Outline each Plasmodium malariae-infected red blood cell.
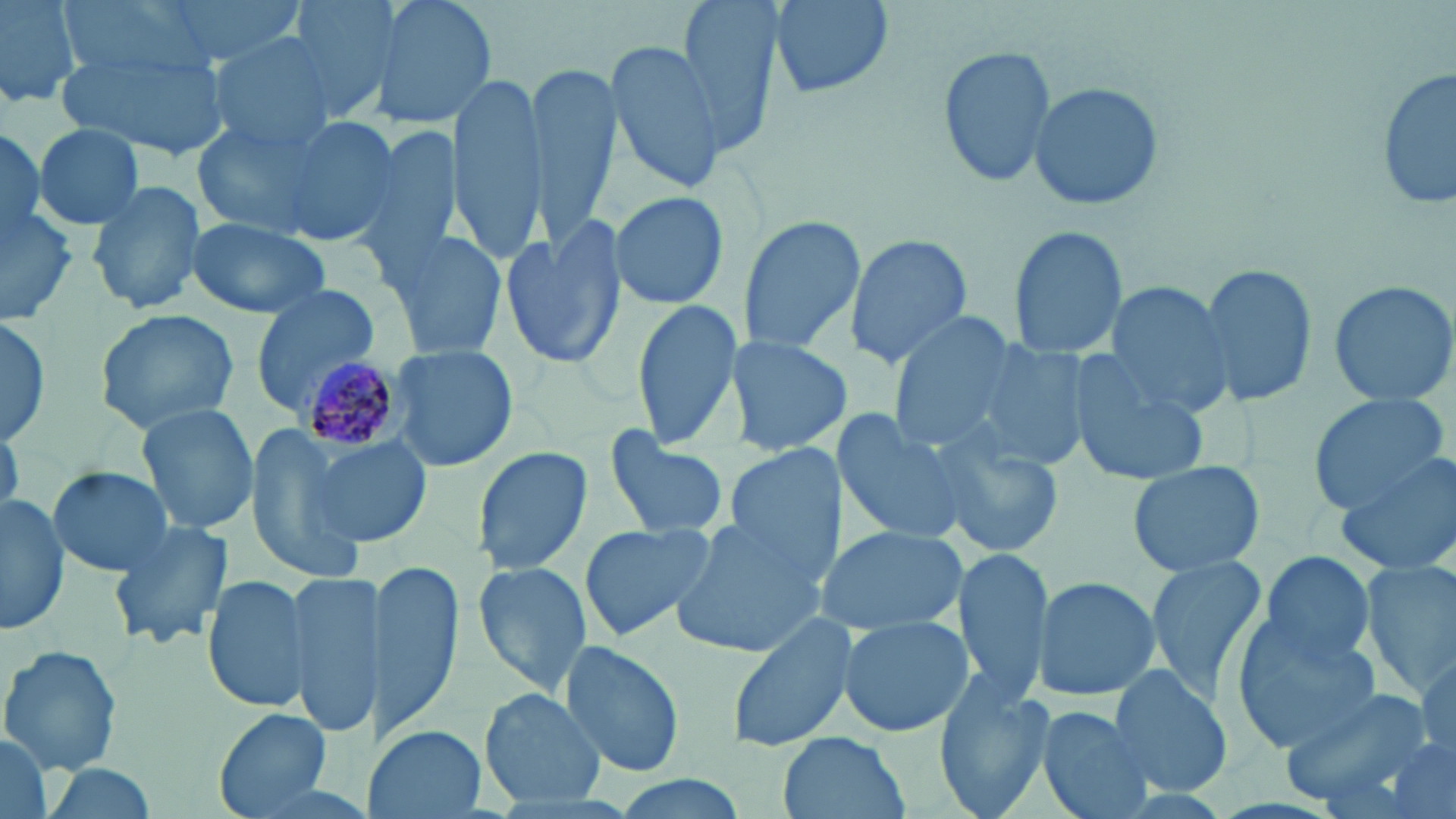

Approximate bounding boxes as named x1/y1/x2/y2 corners in pixels.
Plasmodium malariae-infected red blood cells: (x1=296, y1=355, x2=409, y2=459).

Summary:
  - Uninfected red blood cell locations: (x1=0, y1=0, x2=82, y2=109), (x1=150, y1=0, x2=309, y2=65), (x1=281, y1=0, x2=406, y2=122), (x1=365, y1=0, x2=497, y2=133), (x1=676, y1=0, x2=787, y2=154), (x1=766, y1=0, x2=897, y2=100), (x1=57, y1=35, x2=230, y2=164), (x1=207, y1=35, x2=339, y2=152), (x1=603, y1=36, x2=731, y2=193), (x1=937, y1=45, x2=1058, y2=186), (x1=525, y1=64, x2=618, y2=244), (x1=1377, y1=67, x2=1456, y2=215), (x1=447, y1=71, x2=547, y2=258), (x1=1027, y1=82, x2=1166, y2=212), (x1=192, y1=117, x2=333, y2=240), (x1=269, y1=117, x2=404, y2=249), (x1=353, y1=121, x2=463, y2=276), (x1=0, y1=123, x2=47, y2=243), (x1=32, y1=123, x2=146, y2=230), (x1=87, y1=178, x2=208, y2=317), (x1=609, y1=189, x2=730, y2=312), (x1=0, y1=203, x2=79, y2=322), (x1=735, y1=212, x2=867, y2=357), (x1=499, y1=216, x2=628, y2=372), (x1=185, y1=219, x2=332, y2=319), (x1=1007, y1=225, x2=1129, y2=359), (x1=381, y1=228, x2=509, y2=360), (x1=843, y1=233, x2=972, y2=369), (x1=1199, y1=263, x2=1317, y2=407), (x1=1326, y1=278, x2=1456, y2=405), (x1=1100, y1=280, x2=1238, y2=416), (x1=248, y1=285, x2=381, y2=414), (x1=628, y1=297, x2=743, y2=452), (x1=95, y1=309, x2=240, y2=433), (x1=885, y1=316, x2=1021, y2=451), (x1=0, y1=320, x2=54, y2=447), (x1=729, y1=334, x2=848, y2=460), (x1=972, y1=342, x2=1095, y2=472), (x1=389, y1=344, x2=520, y2=473), (x1=1067, y1=355, x2=1213, y2=483), (x1=1307, y1=393, x2=1451, y2=516), (x1=136, y1=403, x2=260, y2=537), (x1=834, y1=407, x2=974, y2=548), (x1=1, y1=420, x2=23, y2=520), (x1=244, y1=429, x2=366, y2=578), (x1=602, y1=432, x2=730, y2=538), (x1=936, y1=432, x2=1066, y2=558), (x1=303, y1=434, x2=432, y2=549), (x1=724, y1=439, x2=843, y2=587), (x1=473, y1=445, x2=593, y2=574), (x1=1336, y1=450, x2=1456, y2=577), (x1=1125, y1=460, x2=1267, y2=577), (x1=44, y1=464, x2=174, y2=578), (x1=0, y1=493, x2=71, y2=636), (x1=666, y1=511, x2=827, y2=659), (x1=108, y1=516, x2=235, y2=650), (x1=577, y1=521, x2=716, y2=641), (x1=816, y1=525, x2=970, y2=637), (x1=950, y1=546, x2=1052, y2=700), (x1=1259, y1=551, x2=1379, y2=666), (x1=1142, y1=554, x2=1269, y2=702), (x1=1361, y1=559, x2=1455, y2=699), (x1=373, y1=560, x2=464, y2=738), (x1=472, y1=561, x2=592, y2=695), (x1=203, y1=571, x2=315, y2=716), (x1=284, y1=572, x2=386, y2=742), (x1=1031, y1=575, x2=1162, y2=701), (x1=723, y1=612, x2=857, y2=752), (x1=837, y1=613, x2=972, y2=739), (x1=1229, y1=619, x2=1383, y2=754), (x1=556, y1=641, x2=687, y2=778), (x1=1, y1=646, x2=124, y2=774), (x1=1413, y1=653, x2=1455, y2=762), (x1=1106, y1=665, x2=1233, y2=794), (x1=936, y1=668, x2=1057, y2=816), (x1=1278, y1=685, x2=1435, y2=807), (x1=480, y1=689, x2=607, y2=808), (x1=1037, y1=706, x2=1156, y2=819), (x1=212, y1=707, x2=336, y2=816), (x1=367, y1=723, x2=484, y2=819), (x1=0, y1=730, x2=53, y2=819), (x1=776, y1=733, x2=911, y2=819), (x1=1383, y1=740, x2=1454, y2=819), (x1=31, y1=761, x2=163, y2=818), (x1=599, y1=774, x2=755, y2=819)
  - Slide-level diagnosis: Plasmodium malariae
  - Magnification: 1000x
  - Stain: May-Grünwald-Giemsa
  - Preparation: thin blood smear
  - Image size: 1456×819 pixels
  - Modality: light microscopy
  - Field of view: one of a larger specimen